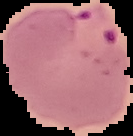
image type = segmented cell region on a black background
image size = 133×136 pixels
malaria status = parasitized
preparation = thin blood film